Report the malaria status of this cell.
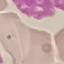

It is uninfected.

Giemsa-stained preparation. Cell patch, automatically extracted from a larger field of view and resized to 64 × 64 pixels. Thin blood smear. Photographed with a smartphone camera at the microscope eyepiece.